Report the malaria status.
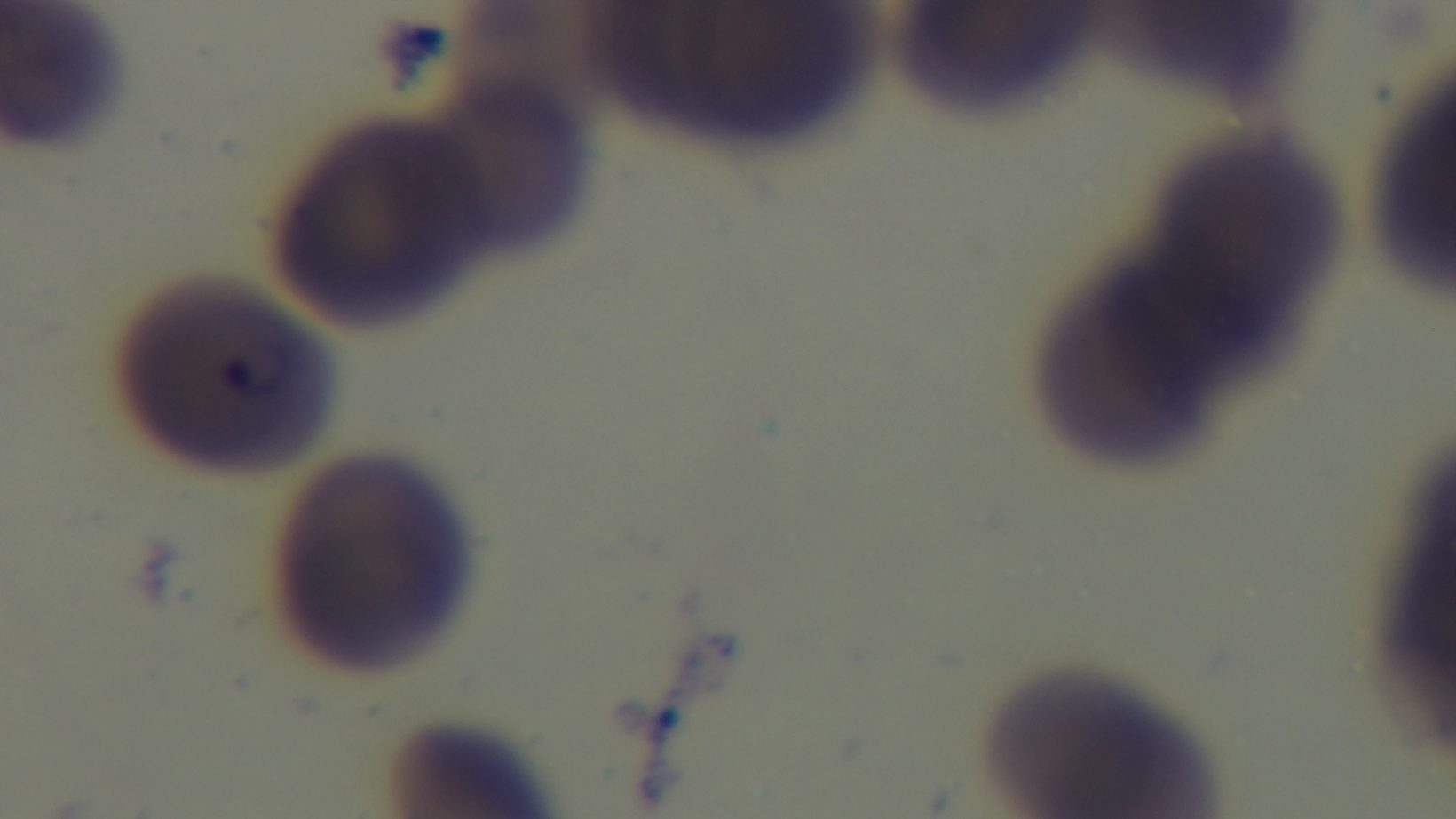
It is infected.

Summary:
  - Capture: mounted 4K digital camera
  - Preparation: thin smear
  - Modality: light microscopy
  - Field of view: single
  - Objective: 100x oil immersion
  - Stain: Giemsa